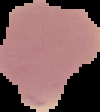

From a thin blood smear. Result: negative for Plasmodium parasites. The area outside the segmented cell region is set to black. Image is 100×112 pixels.